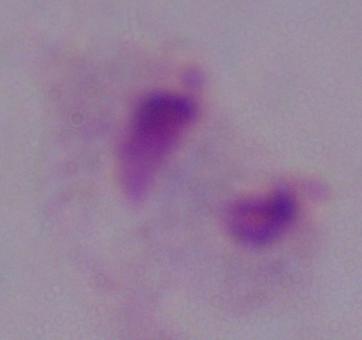

A trichomonad is seen. Captured at 1000x magnification. Micrograph.